Name the parasite shown.
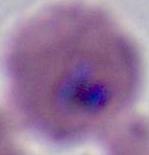

This is Plasmodium.

Summary:
  - Modality: photomicrograph
  - Magnification: 400x or 1000x